Classify this cell by malaria status.
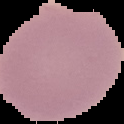

Uninfected.

preparation = thin blood film
image type = cell region segmented out of the field of view; surrounding area masked to black
image size = 124×124 pixels